Classify this cell by malaria status.
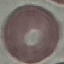
It is uninfected.

Acquired by smartphone through the microscope eyepiece. Giemsa stain. Thin blood film. Automatically extracted cell patch, resized to 64 × 64 pixels.